State which parasite is depicted.
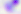
Toxoplasma gondii.

Summary:
  - Modality: micrograph
  - Magnification: 400x